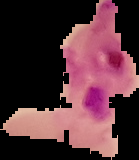
Summary:
  - Image size: 139×160 pixels
  - Image type: segmented cell region with the area outside set to black
  - Preparation: thin blood smear
  - Malaria status: parasitized